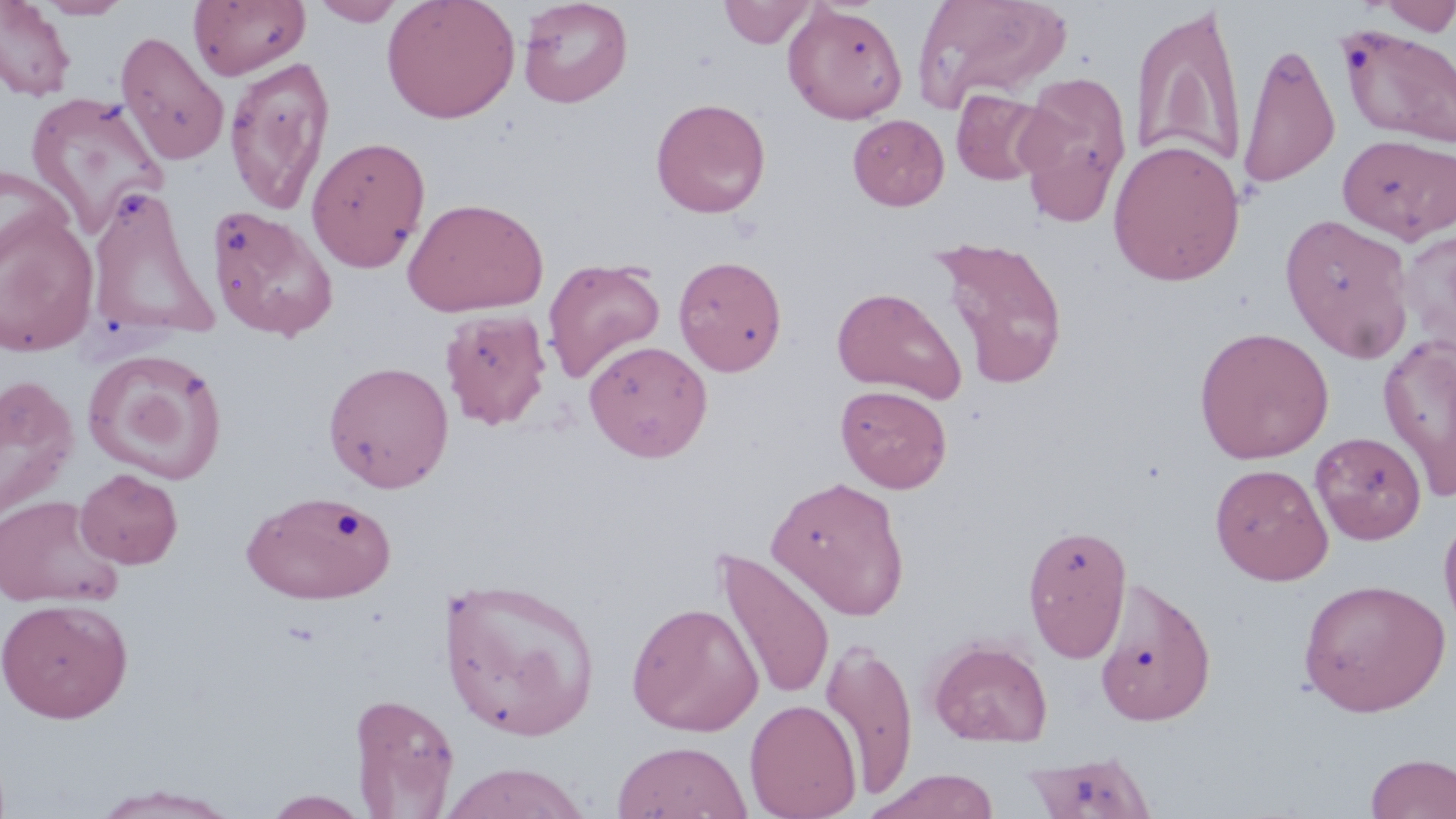

slide_level_diagnosis: negative for blood parasites
image_size: 1456×819 pixels
field_of_view: single
stain: May-Grünwald-Giemsa
preparation: thin blood smear
magnification: 1000x
modality: light microscopy
uninfected_red_blood_cell_locations: 'approximate bounding boxes as (x1,y1)-(x2,y2) corner pairs in pixels: (34,0)-(133,20), (310,0)-(405,26), (382,0)-(520,123), (518,0)-(633,108), (913,0)-(1071,113), (1377,0)-(1455,36), (0,1)-(77,101), (188,1)-(310,80), (719,1)-(819,48), (782,3)-(907,124), (1130,5)-(1249,174), (1339,25)-(1456,148), (115,31)-(230,166), (1237,40)-(1340,190), (224,57)-(336,215), (1014,71)-(1132,226), (951,88)-(1053,185), (25,90)-(171,238), (650,97)-(771,218), (847,114)-(949,210), (1338,133)-(1456,244), (306,135)-(431,272), (1108,138)-(1246,286), (0,163)-(73,272), (86,185)-(217,342), (403,196)-(549,317), (206,204)-(339,342), (0,207)-(99,357), (1280,213)-(1415,364), (1398,229)-(1456,357), (931,235)-(1069,389), (673,255)-(788,376), (543,258)-(666,384), (832,286)-(966,402), (440,308)-(552,430), (1194,327)-(1334,464), (1379,333)-(1456,502), (584,340)-(713,462), (82,349)-(229,485), (323,360)-(454,493), (0,375)-(78,520), (836,384)-(952,493), (1311,431)-(1426,544), (1210,462)-(1333,585), (75,468)-(184,569), (766,475)-(910,619), (242,489)-(397,604), (0,493)-(124,609), (1438,510)-(1456,641), (1023,523)-(1132,662), (714,547)-(835,703), (437,574)-(604,743), (1093,576)-(1217,727), (1297,577)-(1451,716), (0,597)-(134,723), (626,601)-(763,735), (820,634)-(918,799), (927,637)-(1053,747), (348,692)-(459,817), (745,699)-(862,819), (612,741)-(752,819), (1023,750)-(1158,819), (1363,753)-(1456,819), (437,762)-(593,818), (863,769)-(1001,819), (87,785)-(244,818), (262,790)-(371,818)'